Assess this cell for malaria.
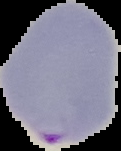

It is parasitized.

preparation: thin blood smear
image_type: cell region segmented out of the field of view; surrounding area masked to black
image_size: 121×151 pixels